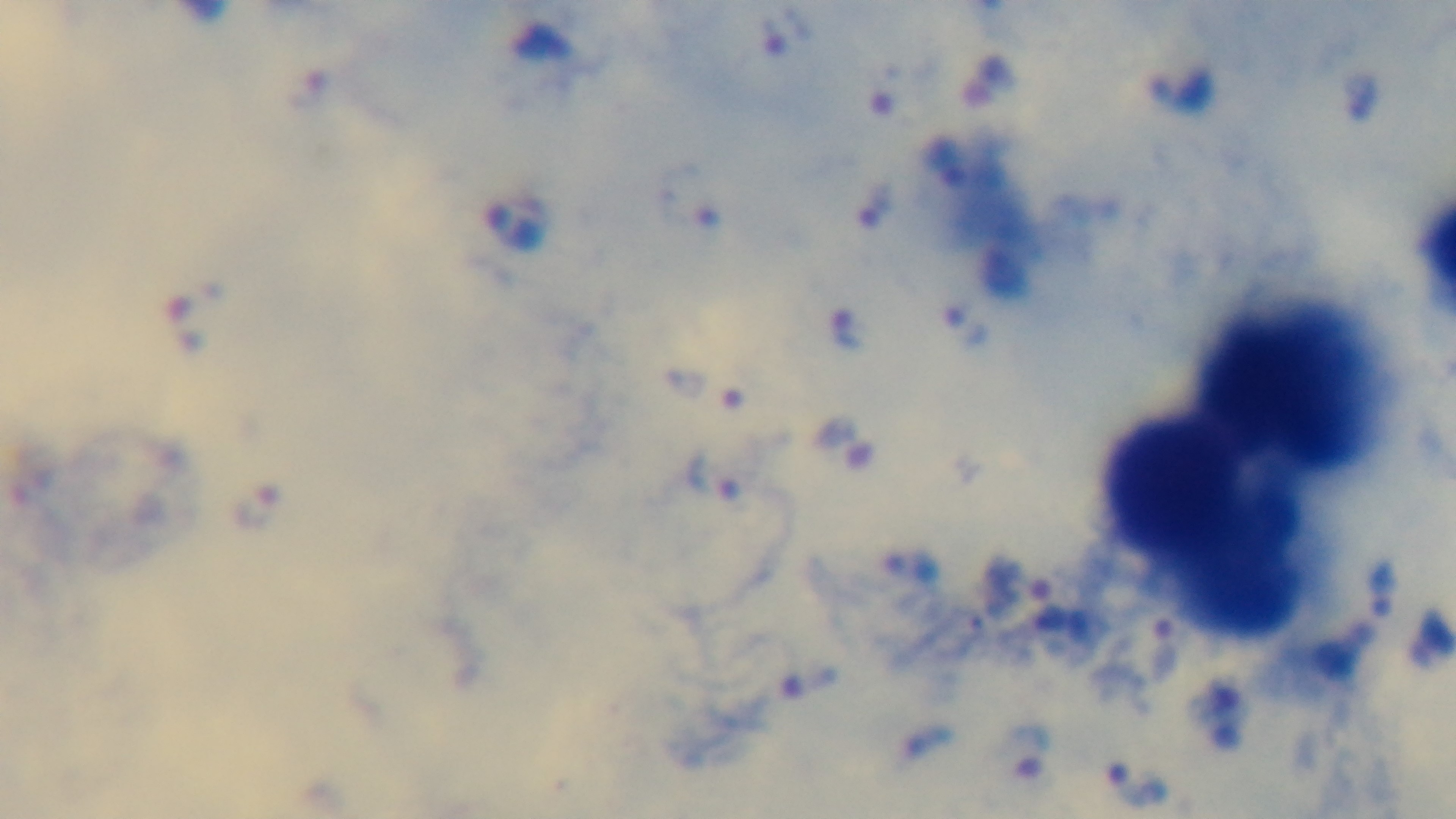
stain = Giemsa
objective = 100x oil immersion
malaria status = infected
modality = light microscopy
field of view = one from the slide
capture = mounted 4K digital camera
preparation = thick smear